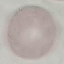
result = negative for malaria parasites
stain = Giemsa
preparation = thin smear
image type = automatically extracted cell patch, resized to 64 × 64 pixels
capture = smartphone camera at the microscope eyepiece